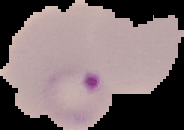
Cell region segmented out of the field of view; the surrounding area is masked to black. From a thin blood film. Result: Plasmodium parasites detected. Image is 184×130 pixels.